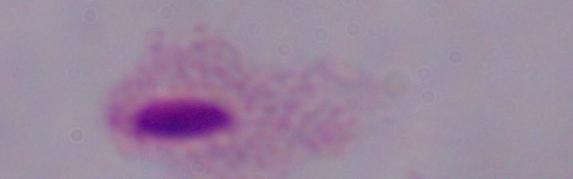
Captured at 1000x magnification. A trichomonad is shown. Photomicrograph.